Report the malaria status of this cell.
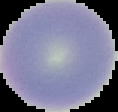
Uninfected.

From a thin blood film. Image is 118×112 pixels. Cell region segmented out of the field of view; the surrounding area is masked to black.